Locate every leukocyte (white blood cell).
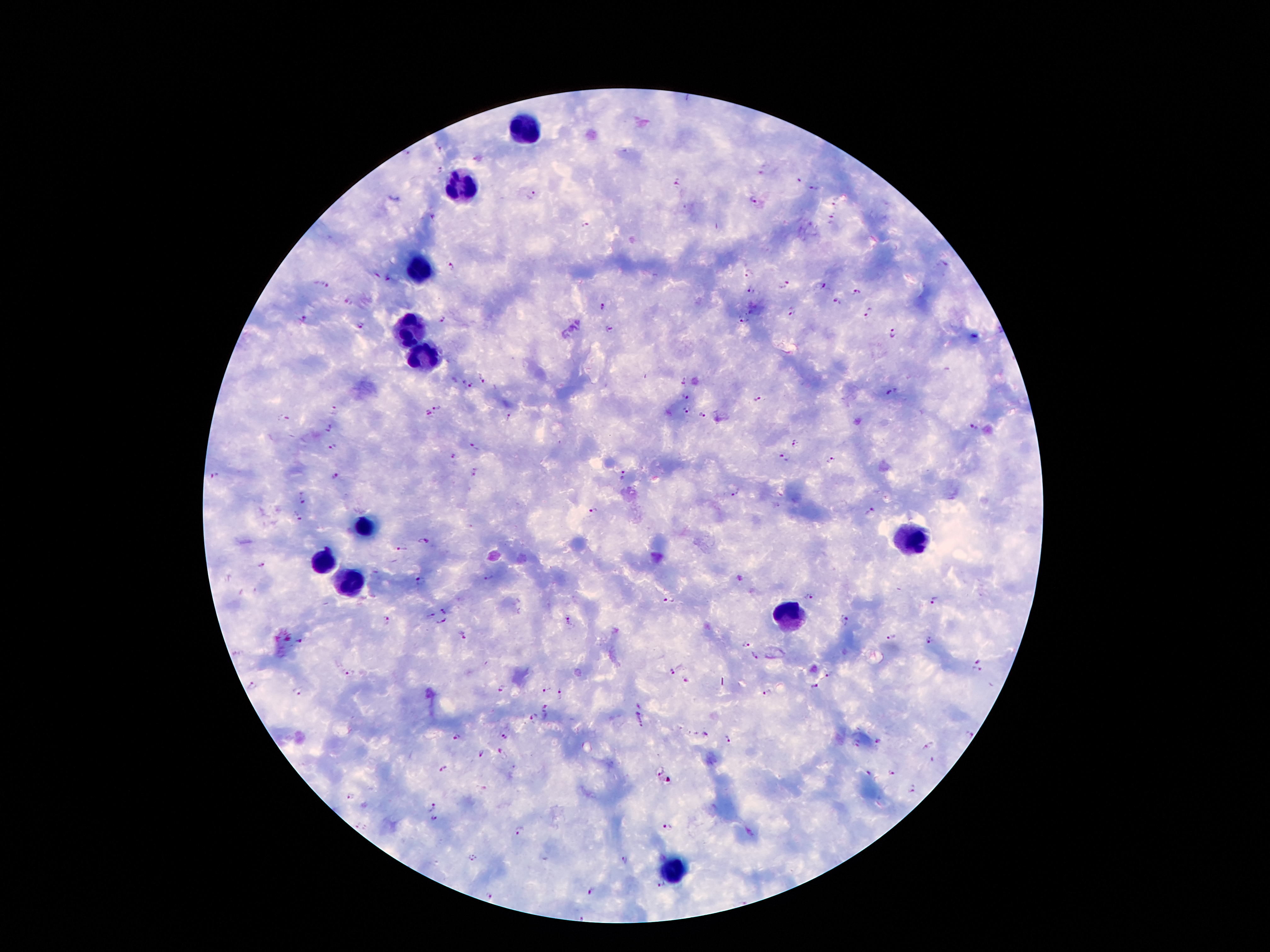
Approximate centers as (x, y) in pixels.
Leukocytes: (521, 128), (460, 184), (424, 268), (409, 329), (417, 353), (366, 526), (911, 539), (323, 561), (348, 584), (793, 618), (673, 872).

Plasmodium parasite locations: (439, 151), (406, 152), (440, 169), (760, 174), (799, 180), (678, 182), (814, 188), (532, 195), (753, 200), (835, 203), (435, 217), (833, 219), (585, 224), (454, 265), (749, 272), (377, 276), (388, 279), (322, 284), (783, 285), (821, 285), (751, 290), (857, 292), (838, 300), (348, 303), (603, 308), (793, 312), (870, 315), (304, 319), (442, 319), (744, 319), (360, 325), (611, 328), (895, 334), (483, 377), (684, 381), (463, 383), (471, 386), (891, 391), (684, 396), (759, 400), (437, 407), (335, 409), (687, 411), (427, 412), (702, 415), (285, 418), (509, 419), (331, 429), (974, 429), (797, 443), (474, 447), (333, 448), (454, 456), (783, 459), (832, 461), (475, 473), (623, 474), (214, 476), (335, 478), (737, 492), (305, 497), (593, 511), (871, 512), (298, 515), (424, 541), (403, 548), (263, 565), (489, 578), (420, 580), (809, 597), (935, 600), (670, 601), (445, 610), (431, 616), (386, 619), (570, 621), (846, 621), (441, 622), (462, 635), (893, 638), (298, 641), (930, 641), (747, 643), (753, 655), (978, 661), (977, 671), (669, 672), (347, 674), (827, 675), (686, 681), (502, 686), (253, 687), (814, 687), (547, 689), (296, 692), (560, 693), (769, 693), (546, 708), (534, 718), (640, 719), (704, 734), (970, 734), (503, 736), (456, 738), (728, 738), (878, 741), (855, 742), (927, 746), (500, 751), (481, 753), (443, 770), (660, 770), (867, 774), (890, 774), (914, 790), (350, 795), (433, 806), (435, 818), (355, 825), (669, 827), (366, 829), (519, 832), (473, 857), (623, 859), (663, 886), (591, 892), (488, 894). Smartphone photograph taken through the microscope eyepiece. Giemsa stain. One field from this slide. 100x magnification. Patient malaria status: infected with Plasmodium falciparum. Thick peripheral-blood smear. Image is 1270×952 pixels.